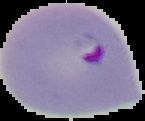
Summary:
  - Image type: segmented cell region with the area outside set to black
  - Image size: 145×121 pixels
  - Preparation: thin blood film
  - Malaria status: parasitized